State which parasite is depicted.
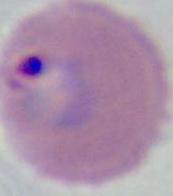

Plasmodium.

Summary:
  - Modality: photomicrograph
  - Magnification: 400x or 1000x